Classify this cell by malaria status.
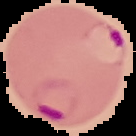
Parasitized.

The area outside the segmented cell region is set to black. Image is 136×136 pixels. From a thin blood smear.